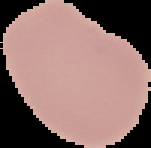
Image is 151×148 pixels. Result: no Plasmodium parasites seen. From a thin blood smear. Cell region segmented out of the field of view; the surrounding area is masked to black.